Assess this cell for malaria.
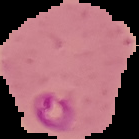

Parasitized.

{
  "image_size": "139×139 pixels",
  "preparation": "thin blood film",
  "image_type": "segmented cell region on a black background"
}